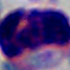

magnification: 1000x
modality: photomicrograph
identification: white blood cell